Describe the morphology of the erythrocytes.
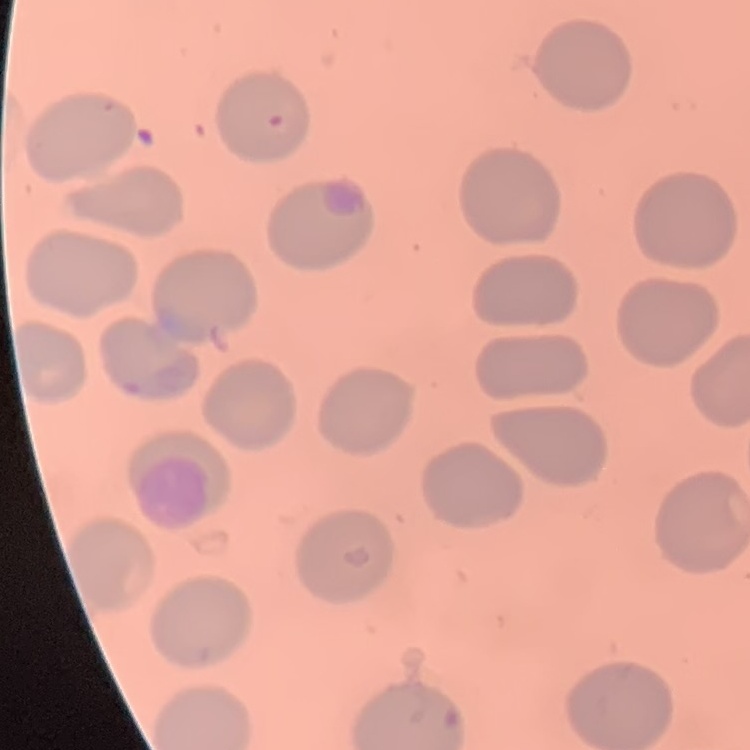

They show no rouleaux formation.

image type = one tile cut from a larger photomicrograph
stain = Field's or Giemsa
preparation = thin blood film